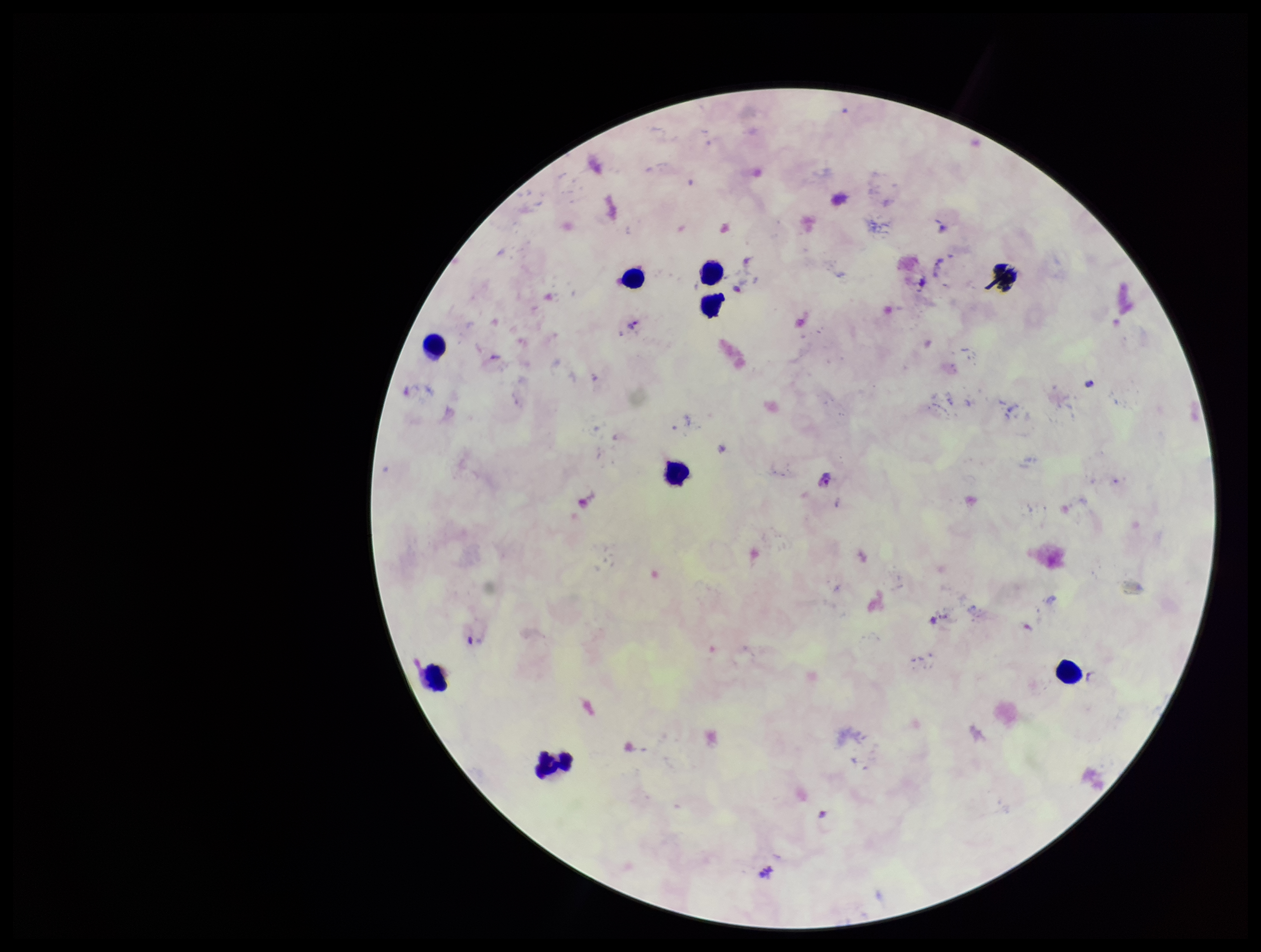
image size = 1261×952 pixels
capture = smartphone photograph through the microscope eyepiece
Plasmodium parasites = detected
field of view = single
leukocyte count = 8
stain = Giemsa
parasite count = 2
species reported for this patient = Plasmodium falciparum
preparation = thick smear
patient malaria status = infected